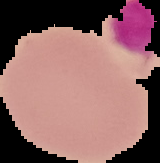
Summary:
  - Image type: cell region segmented out of the field of view; surrounding area masked to black
  - Image size: 160×163 pixels
  - Result: negative for malaria parasites
  - Preparation: thin blood film